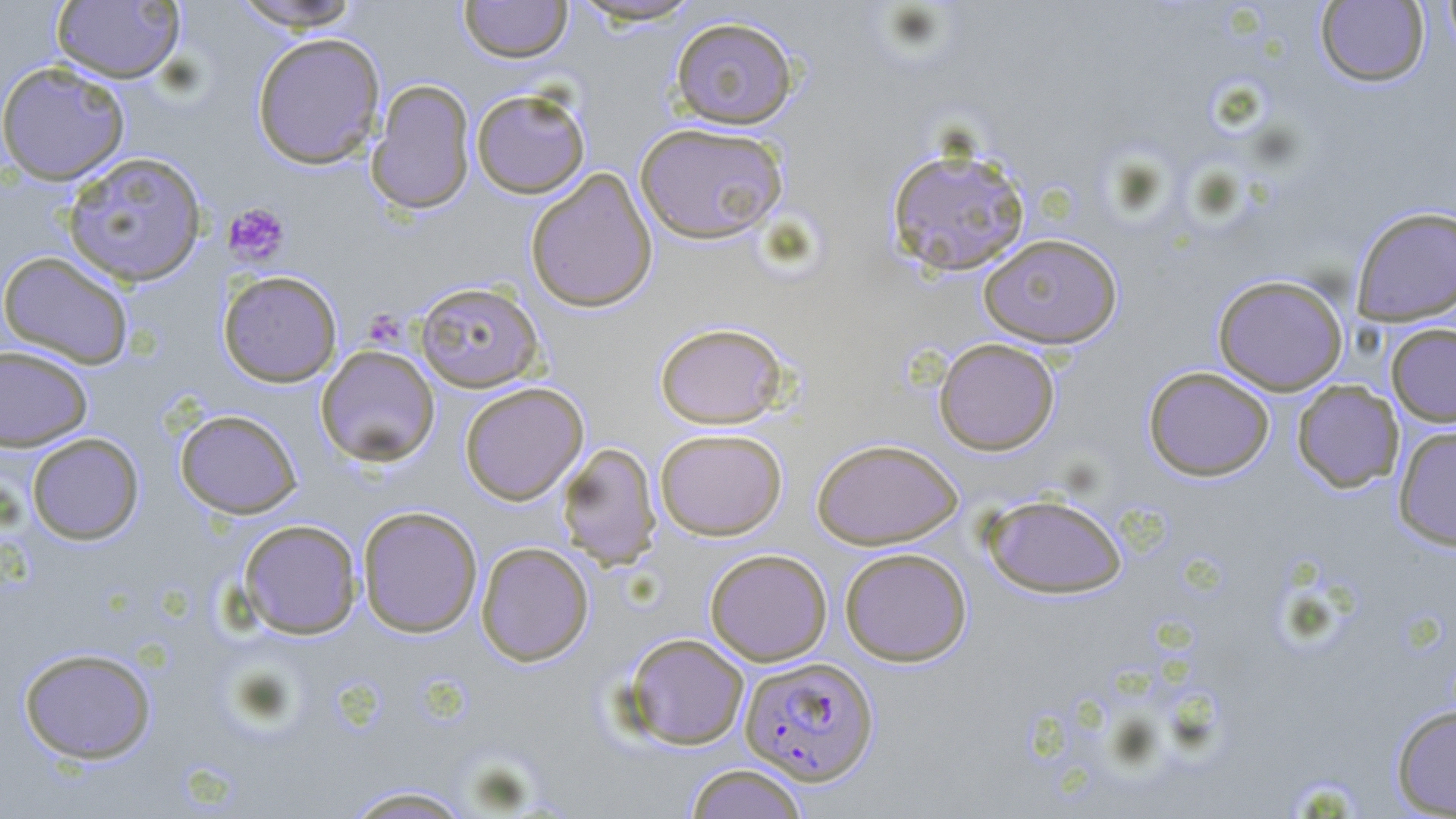

Summary:
  - Coordinate format: approximate bounding boxes as [x1, y1, x2, y2] in pixels
  - Platelet locations: [222, 202, 290, 267], [366, 305, 412, 356]
  - Plasmodium falciparum-infected red blood cell locations: [739, 656, 879, 785]
  - Uninfected red blood cell locations: [228, 0, 365, 31], [459, 0, 572, 63], [568, 0, 705, 27], [1441, 0, 1456, 58], [50, 1, 186, 84], [1315, 1, 1430, 87], [670, 15, 798, 130], [251, 31, 386, 169], [0, 60, 131, 185], [366, 79, 476, 215], [470, 87, 591, 199], [634, 122, 788, 245], [886, 144, 1031, 277], [62, 151, 208, 287], [525, 168, 658, 313], [1351, 206, 1456, 326], [978, 233, 1123, 348], [0, 251, 135, 368], [218, 270, 343, 387], [1212, 274, 1349, 395], [415, 281, 544, 392], [654, 321, 790, 429], [1386, 323, 1456, 427], [934, 337, 1060, 455], [0, 345, 94, 452], [315, 345, 440, 467], [1143, 366, 1274, 481], [1292, 380, 1403, 493], [459, 382, 588, 505], [175, 409, 302, 519], [1393, 424, 1456, 550], [655, 428, 788, 541], [26, 432, 144, 545], [812, 438, 963, 549], [557, 442, 661, 569], [982, 494, 1127, 599], [357, 505, 483, 638], [237, 519, 363, 639], [475, 541, 594, 667], [839, 547, 972, 666], [704, 548, 832, 666], [622, 632, 750, 750], [18, 646, 157, 764], [1390, 704, 1456, 817], [684, 763, 808, 819], [340, 784, 476, 818]
  - Slide-level diagnosis: Plasmodium falciparum
  - Field of view: single
  - Modality: light microscopy
  - Stain: May-Grünwald-Giemsa
  - Magnification: 1000x
  - Image size: 1456×819 pixels
  - Preparation: thin blood film